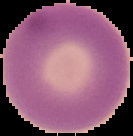

image size = 133×136 pixels
result = no Plasmodium parasites seen
image type = segmented cell region on a black background
preparation = thin blood film